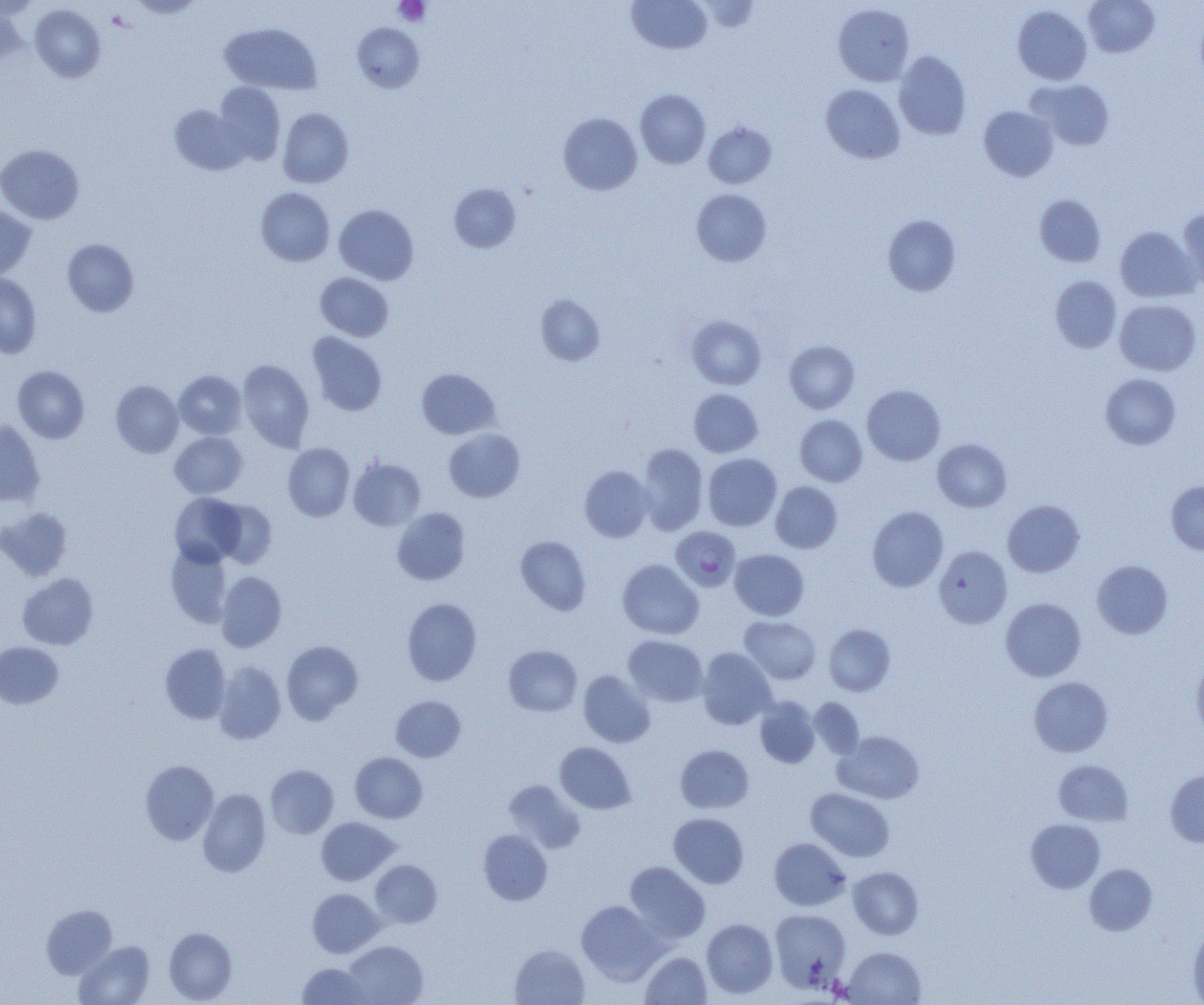

Approximate bounding boxes as (x1,y1)-(x2,y2) corner pairs in pixels. Uninfected red blood cell locations: (627,0)-(712,54), (1084,0)-(1159,57), (698,1)-(759,32), (833,3)-(915,86), (29,4)-(105,82), (1013,5)-(1092,84), (0,6)-(23,68), (1195,11)-(1204,90), (220,23)-(322,94), (353,23)-(424,92), (894,51)-(971,140), (1027,79)-(1114,150), (214,82)-(285,164), (821,84)-(905,164), (635,89)-(711,169), (169,104)-(249,175), (979,106)-(1058,181), (278,108)-(353,188), (558,112)-(642,195), (704,121)-(776,188), (0,145)-(84,224), (449,183)-(521,253), (256,187)-(335,266), (691,189)-(772,266), (1034,194)-(1106,267), (334,204)-(419,284), (0,205)-(36,280), (1178,208)-(1204,291), (883,215)-(961,295), (1115,227)-(1199,302), (62,239)-(139,316), (0,272)-(41,358), (315,272)-(394,341), (1050,275)-(1121,353), (536,294)-(605,365), (1114,299)-(1202,376), (686,315)-(766,390), (307,332)-(387,416), (784,340)-(859,413), (238,360)-(314,451), (13,365)-(89,443), (416,368)-(500,439), (174,370)-(246,439), (1100,373)-(1181,450), (111,380)-(183,457), (862,384)-(945,466), (688,388)-(763,457), (795,415)-(867,487), (0,420)-(45,506), (444,428)-(525,502), (170,432)-(247,498), (932,438)-(1012,512), (283,443)-(354,521), (637,444)-(707,535), (703,453)-(782,530), (349,457)-(425,530), (580,466)-(653,542), (1166,481)-(1204,554), (770,482)-(842,553), (170,492)-(247,567), (215,499)-(277,568), (1002,500)-(1085,577), (867,506)-(948,591), (0,507)-(73,580), (392,507)-(470,585), (515,535)-(590,615), (166,542)-(232,627), (934,545)-(1012,629), (730,549)-(809,620), (617,559)-(703,639), (1092,560)-(1173,639), (216,571)-(286,652), (18,573)-(98,649), (402,598)-(482,685), (1001,598)-(1086,681), (740,616)-(821,684), (824,624)-(895,696), (623,635)-(708,707), (282,641)-(362,723), (0,642)-(63,708), (160,644)-(230,723), (503,645)-(582,716), (697,648)-(777,729), (1191,655)-(1204,740), (214,661)-(286,744), (578,670)-(655,748), (1029,677)-(1113,757), (391,695)-(466,762), (755,697)-(820,768), (808,697)-(864,758), (834,731)-(924,804), (555,742)-(636,814), (675,745)-(754,813), (350,752)-(427,823), (140,760)-(219,845), (1053,760)-(1133,826), (266,765)-(338,838), (1165,769)-(1204,848), (504,780)-(585,853), (198,788)-(271,877), (807,788)-(894,861), (669,813)-(749,888), (316,817)-(399,885), (1026,818)-(1106,893), (477,829)-(552,905), (770,837)-(850,910), (370,860)-(442,927), (624,861)-(710,944), (1084,863)-(1157,935), (848,867)-(923,939), (307,888)-(384,957), (576,900)-(664,984), (41,904)-(117,978), (770,909)-(851,992), (702,919)-(778,998), (1188,925)-(1204,1004), (164,927)-(237,1003), (344,940)-(428,1005), (74,941)-(155,1005), (509,944)-(590,1005), (843,947)-(925,1004), (640,951)-(711,1004), (298,962)-(371,1004). Platelet locations: (394,0)-(431,26). Plasmodium falciparum-infected red blood cell locations: (673,527)-(743,592). Slide-level diagnosis: Plasmodium falciparum. Single field of view. 1000x magnification. Thin blood smear. Light microscopy. Image is 1204×1005 pixels.